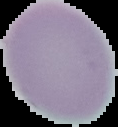

image type = segmented cell region on a black background
image size = 118×127 pixels
result = no Plasmodium parasites detected
preparation = thin blood smear